Assess the morphology of the red blood cells.
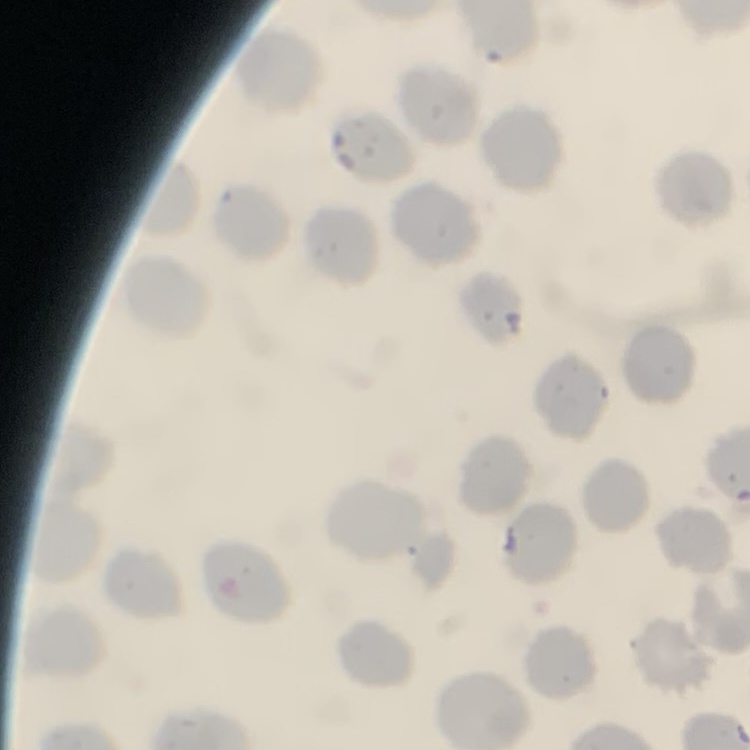
No rouleaux formation.

{
  "preparation": "thin blood smear",
  "stain": "Field's or Giemsa",
  "image_type": "one tile cut from a larger photomicrograph"
}